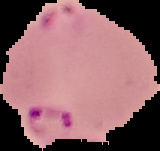 From a thin blood film. Image is 160×151 pixels. Segmented cell region on a black background. Malaria status: parasitized.